Identify the parasite.
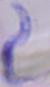
This is a trypanosome.

Summary:
  - Modality: micrograph
  - Magnification: 1000x